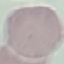

Summary:
  - Malaria status: uninfected
  - Image type: automatically extracted cell patch, resized to 64 × 64 pixels
  - Stain: Giemsa
  - Preparation: thin smear
  - Capture: smartphone through the microscope eyepiece